Name the parasite shown.
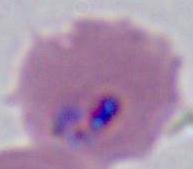
This is Plasmodium.

400x or 1000x magnification. Micrograph.